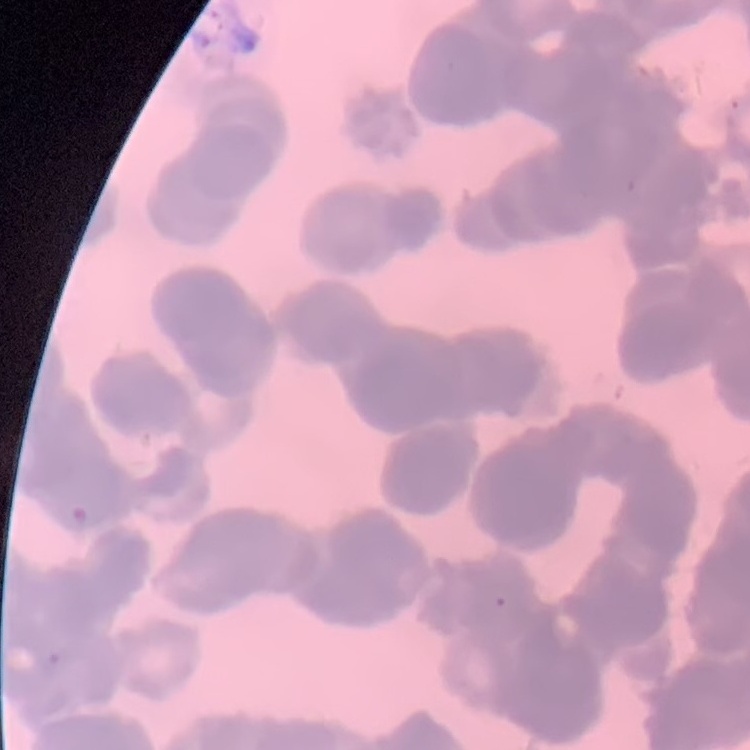
{
  "red_blood_cell_morphology": "rouleaux formation",
  "preparation": "thin blood smear",
  "image_type": "square crop of a larger photomicrograph",
  "stain": "Field's or Giemsa"
}